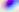 Captured at 400x magnification. Toxoplasma gondii is seen. Micrograph.